Report the malaria status of this cell.
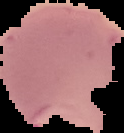

Parasitized.

image type = segmented cell region with the area outside set to black
image size = 124×133 pixels
preparation = thin blood film